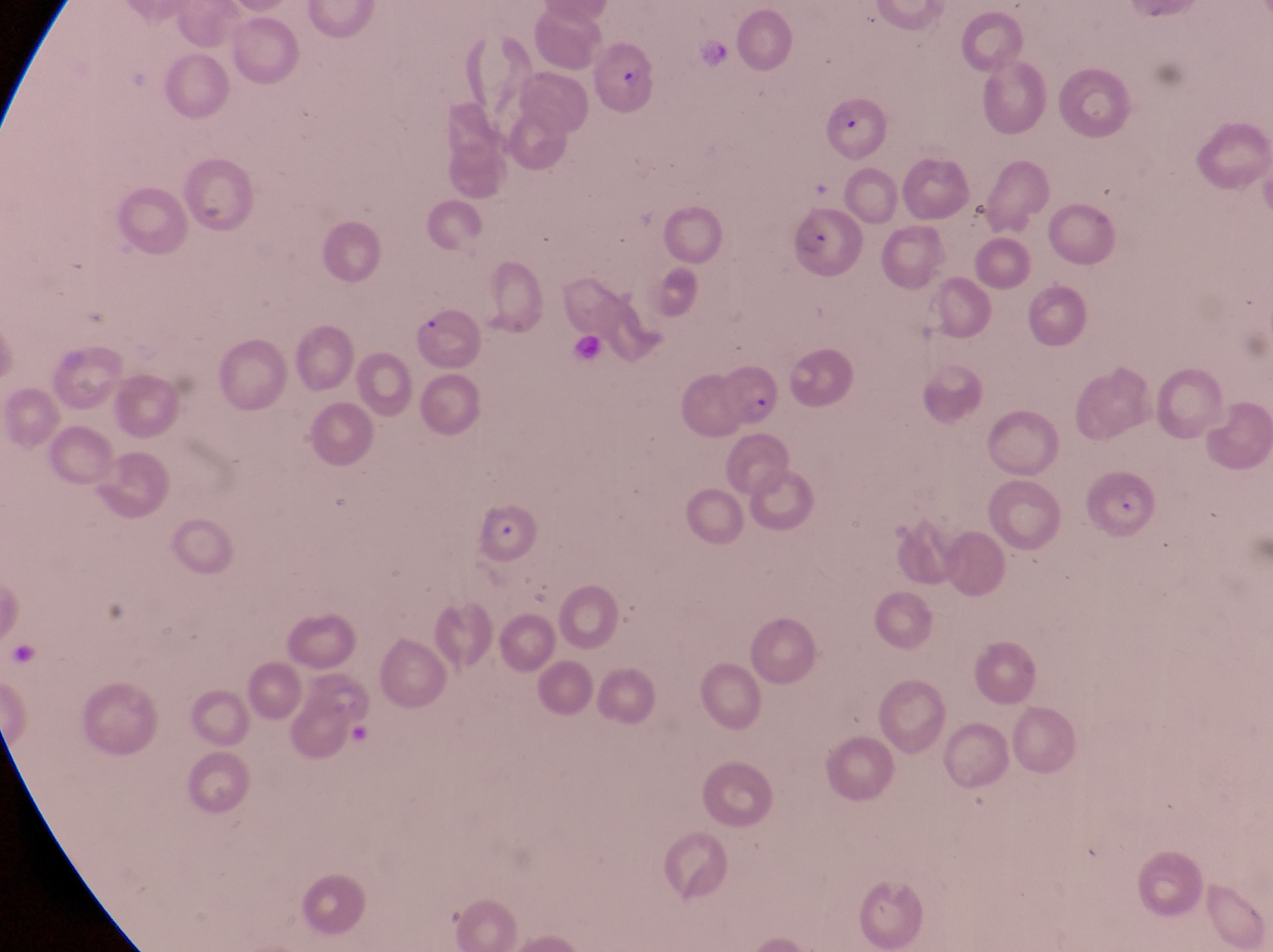

country = Uganda
preparation = thin blood smear
parasitised red blood cell locations = approximate bounding boxes as left top right bottom in pixels: 591 40 665 122; 828 90 890 167; 787 204 864 281; 717 365 782 423; 1091 469 1160 539; 477 499 547 569
field of view = single
image size = 1273×952 pixels
capture = smartphone photograph through the eyepiece of an Olympus CX-23 microscope
magnification = 1000x